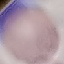 Result: no malaria parasites detected. Automatically extracted cell patch, resized to 64 × 64 pixels. Photographed with a smartphone camera at the microscope eyepiece. Thin smear of blood. Giemsa-stained preparation.